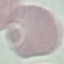

Summary:
  - Result: negative for malaria parasites
  - Stain: Giemsa
  - Image type: automatically extracted cell patch, resized to 64 × 64 pixels
  - Capture: smartphone camera at the microscope eyepiece
  - Preparation: thin blood film